Give the position of every malaria parasite.
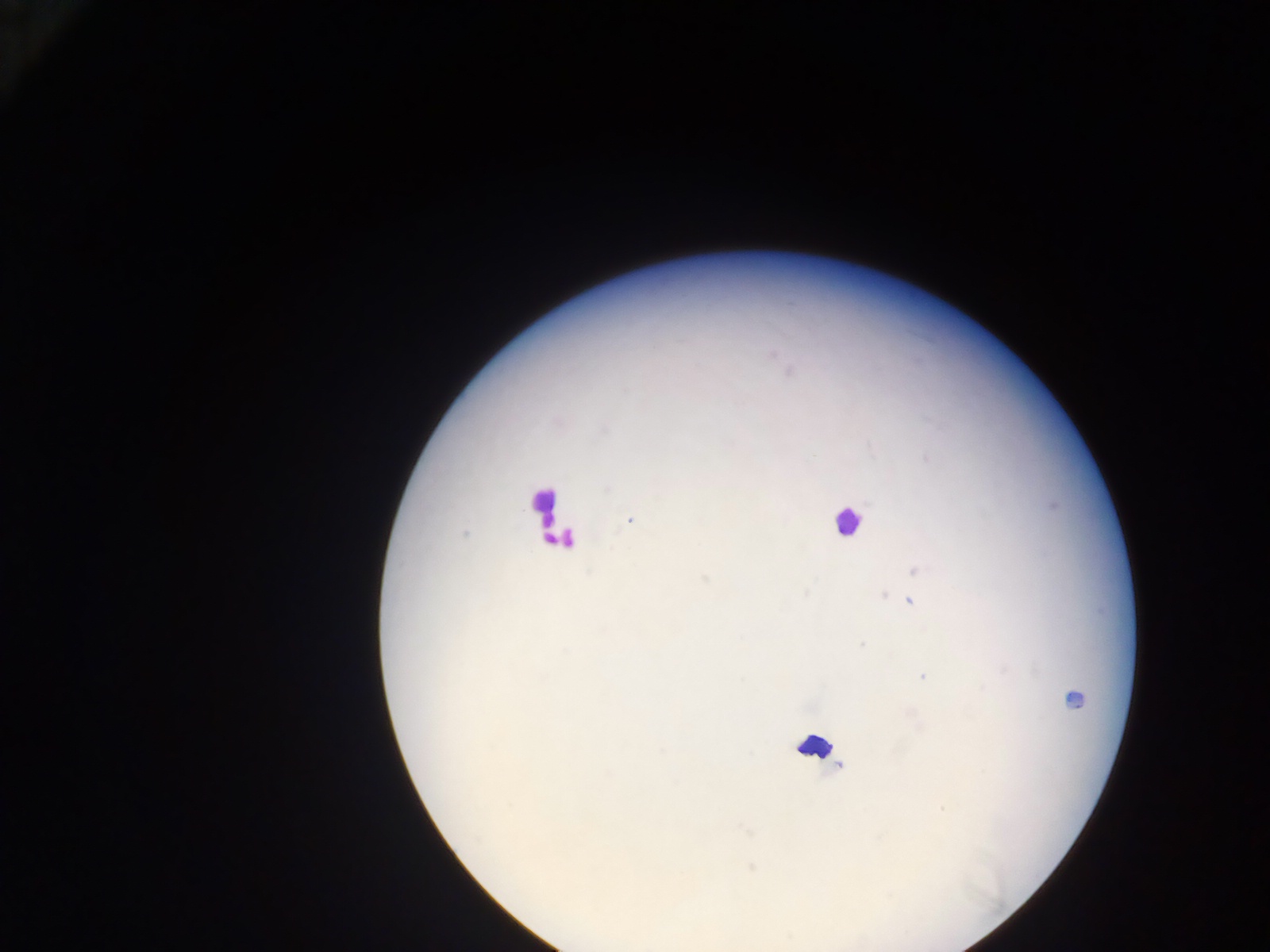
Approximate centers as [x, y] in pixels.
Malaria parasites: [630, 521], [465, 533], [914, 570], [705, 578], [806, 593], [883, 595], [897, 597], [910, 601], [862, 644], [922, 676], [943, 809].

Summary:
  - Leukocyte locations (subset; some below the resolvable size): [543, 502], [846, 521], [554, 538], [1074, 700], [818, 746]
  - Preparation: thick blood film
  - Capture: mobile-phone photograph through a microscope
  - Country: Ghana
  - Image size: 1270×952 pixels
  - Field of view: single